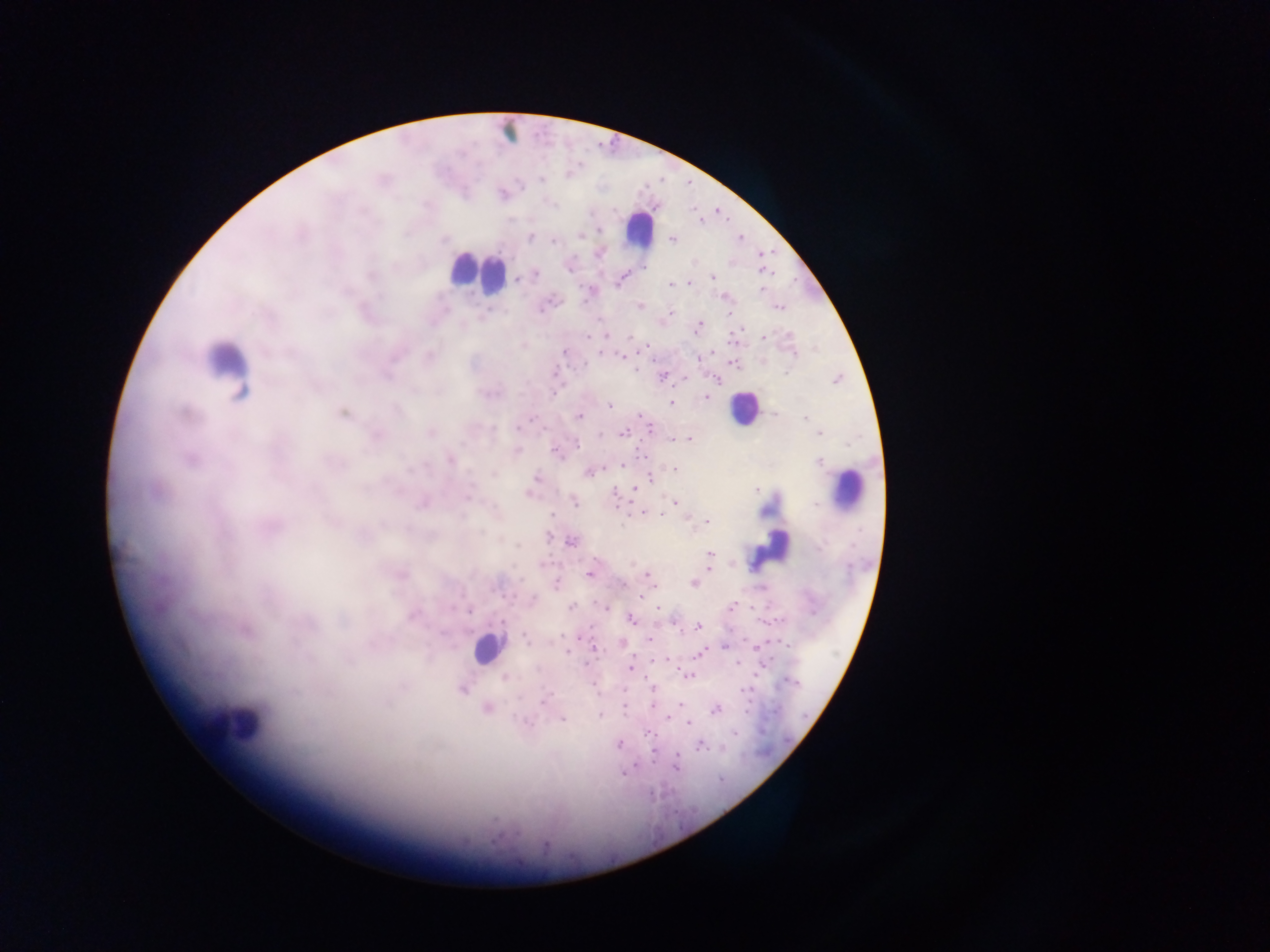 Approximate centers as (x, y) in pixels. Malaria parasite locations: (540, 179), (502, 194), (581, 233), (528, 237), (672, 239), (554, 240), (599, 252), (761, 273), (536, 274), (713, 276), (516, 279), (620, 279), (689, 282), (670, 285), (761, 290), (591, 291), (725, 296), (640, 306), (778, 307), (667, 314), (697, 325), (606, 335), (763, 336), (588, 337), (523, 345), (646, 345), (565, 351), (600, 353), (621, 356), (428, 357), (699, 358), (733, 362), (635, 367), (662, 376), (838, 379), (714, 380), (705, 396), (671, 403), (608, 406), (343, 413), (772, 413), (640, 414), (579, 416), (804, 417), (651, 430), (430, 431), (819, 432), (624, 433), (375, 435), (671, 438), (688, 438), (516, 451), (643, 455), (189, 458), (450, 459), (622, 463), (674, 469), (589, 472), (649, 473), (535, 478), (634, 489), (530, 493), (614, 493), (675, 501), (423, 502), (574, 502), (645, 513), (552, 515), (705, 521), (269, 526), (571, 542), (710, 553), (709, 567), (589, 573), (400, 574), (648, 575), (692, 583), (556, 584), (640, 599), (532, 600), (570, 606), (604, 606), (732, 606), (412, 614), (630, 619), (502, 622), (697, 627), (244, 630), (647, 639), (621, 643), (725, 644), (593, 648), (699, 652), (566, 653), (652, 661), (736, 663), (631, 667), (686, 675), (504, 677), (652, 685), (461, 688), (545, 698), (678, 702), (654, 705), (623, 706), (487, 708), (714, 709), (599, 715), (668, 717), (561, 718), (526, 723), (688, 723), (647, 732), (734, 733), (618, 743), (701, 745), (654, 751), (677, 761), (623, 772). Leukocyte locations: (507, 130), (639, 230), (476, 272), (225, 369), (743, 408), (847, 490), (770, 549), (488, 648), (237, 723). Collected in Ghana. Single field of view. Image is 1270×952 pixels. Thick blood film. Photographed through a microscope with a mobile-phone camera.